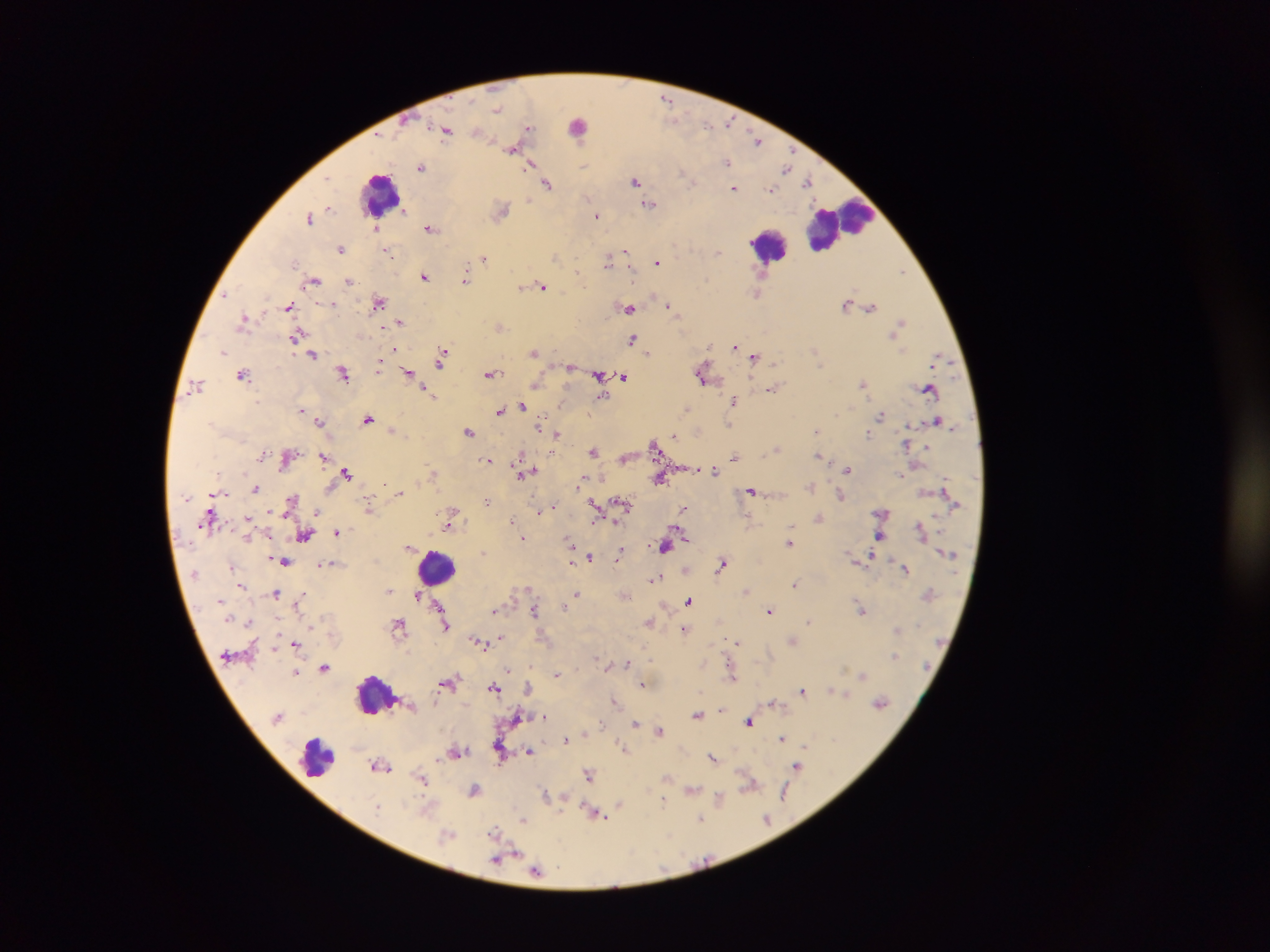
Approximate centers as x y in pixels. Malaria parasite locations: 666 98; 729 122; 529 128; 447 129; 757 140; 513 147; 726 162; 532 163; 423 167; 787 168; 636 180; 808 181; 547 184; 735 187; 772 189; 649 204; 502 209; 597 215; 311 218; 375 226; 430 227; 341 249; 386 249; 626 250; 718 251; 484 257; 608 260; 657 261; 901 271; 425 276; 349 280; 466 280; 313 281; 522 286; 543 287; 759 293; 226 294; 378 302; 847 302; 333 304; 670 305; 289 306; 870 306; 630 307; 245 318; 401 321; 900 324; 500 326; 896 331; 297 335; 633 339; 736 344; 223 351; 535 352; 648 352; 313 354; 442 355; 754 357; 939 357; 380 366; 570 367; 344 372; 409 372; 703 373; 243 374; 490 374; 600 375; 622 377; 535 384; 863 384; 196 385; 772 388; 930 389; 427 391; 602 394; 734 400; 522 405; 301 408; 688 409; 500 410; 880 415; 368 418; 937 420; 320 422; 729 425; 540 427; 393 431; 817 431; 470 432; 557 433; 869 434; 674 435; 907 443; 655 445; 776 449; 594 450; 324 455; 820 455; 287 456; 735 456; 625 458; 489 460; 847 468; 714 470; 433 471; 525 471; 347 473; 534 473; 901 474; 660 477; 582 479; 385 483; 811 487; 256 489; 752 491; 400 493; 841 495; 292 500; 487 502; 595 503; 623 503; 550 508; 684 508; 369 509; 540 510; 318 511; 453 512; 883 512; 451 519; 512 519; 596 519; 819 519; 615 520; 448 526; 339 530; 922 530; 306 535; 682 535; 880 536; 523 538; 790 542; 571 545; 665 545; 410 548; 482 552; 621 553; 591 557; 869 558; 573 559; 284 561; 325 563; 723 564; 233 566; 687 568; 906 568; 656 577; 795 583; 242 584; 528 588; 390 590; 747 590; 276 592; 577 593; 302 595; 418 595; 626 595; 688 600; 298 604; 440 606; 564 607; 861 609; 495 610; 534 610; 770 611; 809 621; 649 622; 446 624; 399 625; 312 627; 685 629; 898 630; 501 637; 793 639; 737 641; 479 642; 297 644; 894 655; 627 663; 609 665; 324 667; 509 669; 297 672; 557 674; 862 675; 733 677; 448 682; 642 683; 494 686; 529 687; 838 691; 803 692; 844 694; 615 700; 773 703; 881 703; 721 708; 699 714; 518 716; 543 716; 749 721; 601 723; 636 723; 659 731; 585 733; 783 738; 566 739; 624 747; 500 749; 530 751; 457 752; 440 758; 713 758; 380 765; 798 765; 589 773; 423 779; 750 784; 475 789; 692 791; 785 792; 546 794; 564 797; 721 797; 664 799; 620 804; 378 805; 597 812; 559 813; 701 819; 767 819; 523 820; 495 832; 536 870. Leukocyte locations: 579 125; 380 193; 838 223; 769 245; 437 567; 375 694; 317 757. Image is 1270×952 pixels. Mobile-phone photograph taken through the microscope. Thick blood smear. One field of view. Collected in Ghana.